State which cell type is depicted.
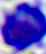
This is a leukocyte.

{
  "magnification": "400x",
  "modality": "photomicrograph"
}